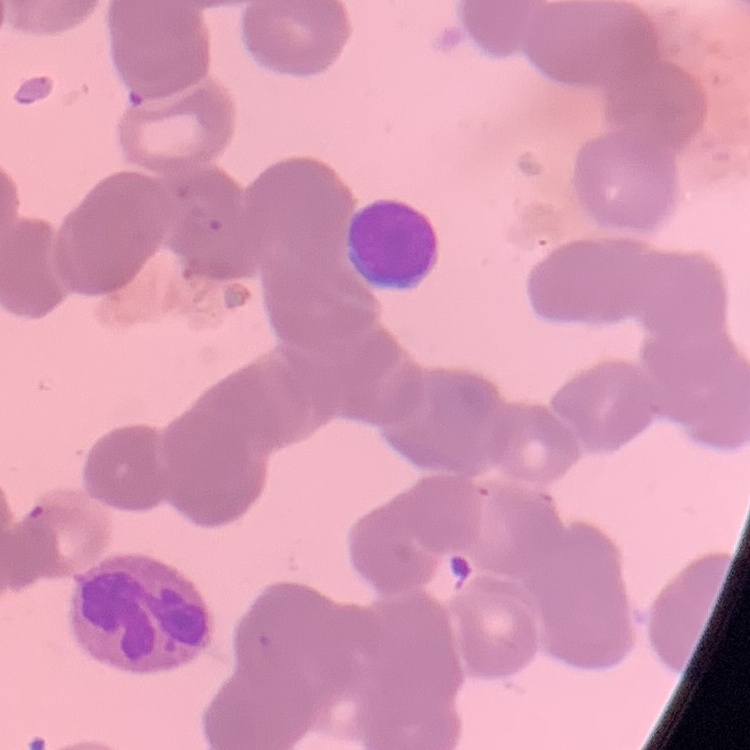 The red blood cells show rouleaux formation. Square crop of a larger photomicrograph. Thin blood film. Stained with either Field's or Giemsa.